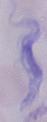

modality = micrograph
identification = trypanosome
magnification = 1000x